Identify the parasite.
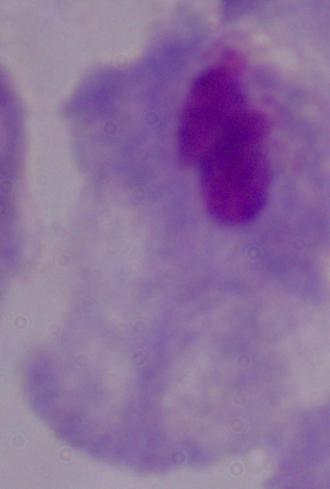
A trichomonad.

modality = photomicrograph
magnification = 1000x